Give the position of every malaria parasite and every leukocyte.
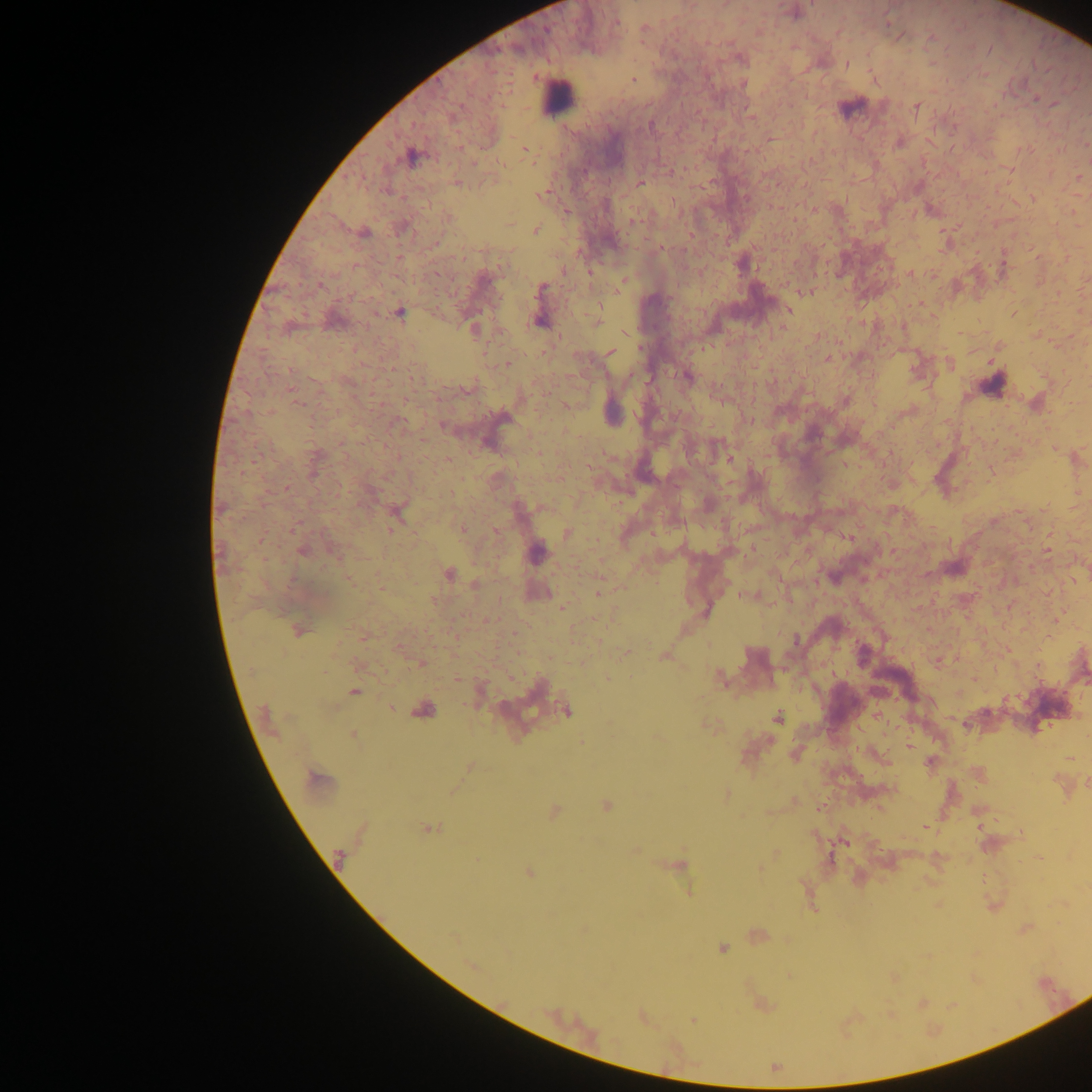

Approximate centers as (x, y) in pixels.
Malaria parasites: (887, 22), (930, 37), (971, 47), (848, 65), (983, 73), (633, 78), (742, 84), (1035, 99), (1054, 104), (917, 106), (954, 129), (459, 147), (524, 147), (406, 156), (812, 161), (474, 163), (924, 163), (501, 164), (458, 183), (641, 183), (1033, 199), (777, 207), (567, 210), (536, 229), (691, 233), (662, 247), (354, 265), (563, 270), (590, 273), (909, 274), (319, 284), (542, 287), (919, 302), (788, 311), (400, 312), (625, 333), (818, 336), (611, 353), (827, 358), (509, 363), (291, 371), (688, 377), (290, 390), (300, 405), (566, 406), (1055, 447), (729, 459), (590, 467), (992, 472), (243, 473), (288, 489), (462, 527), (392, 529), (495, 531), (1047, 550), (450, 575), (597, 594), (561, 608), (423, 663), (1038, 667), (607, 677), (719, 677), (353, 691), (390, 707), (419, 711), (778, 718), (353, 735), (908, 746), (727, 793), (428, 827), (978, 827), (924, 828), (634, 853), (1039, 857), (476, 859), (529, 874), (722, 948), (692, 1020).
Leukocytes: (559, 97).

Photographed through a microscope with a mobile-phone camera. Single field of view. Image is 1092×1092 pixels. Thick blood smear. Sample from Ghana.